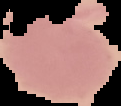
malaria status = uninfected
image type = segmented cell region on a black background
preparation = thin blood film
image size = 121×106 pixels